Assess the morphology of the erythrocytes.
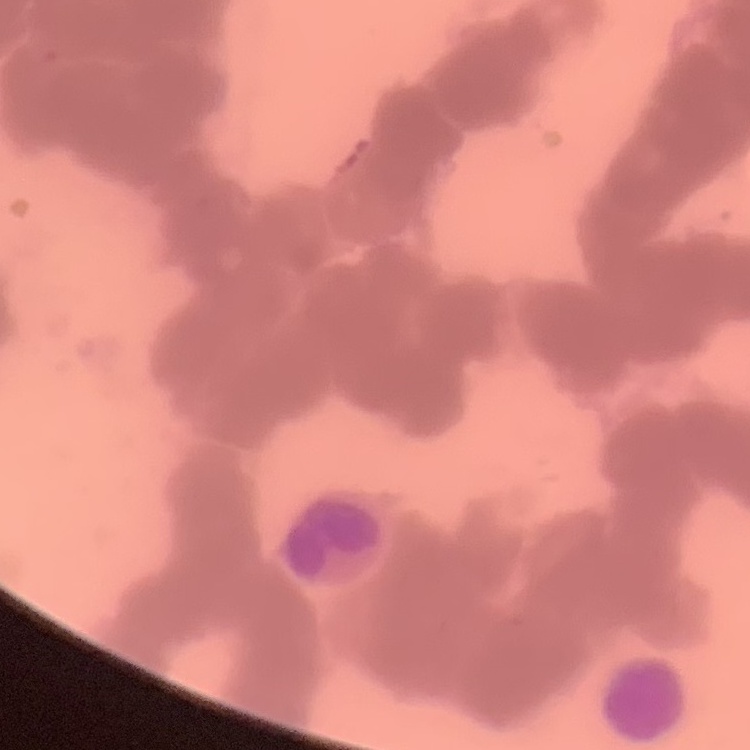
They show rouleaux formation.

Summary:
  - Stain: Field's or Giemsa
  - Image type: square crop of a larger photomicrograph
  - Preparation: thin blood film